Assess the morphology of the red blood cells.
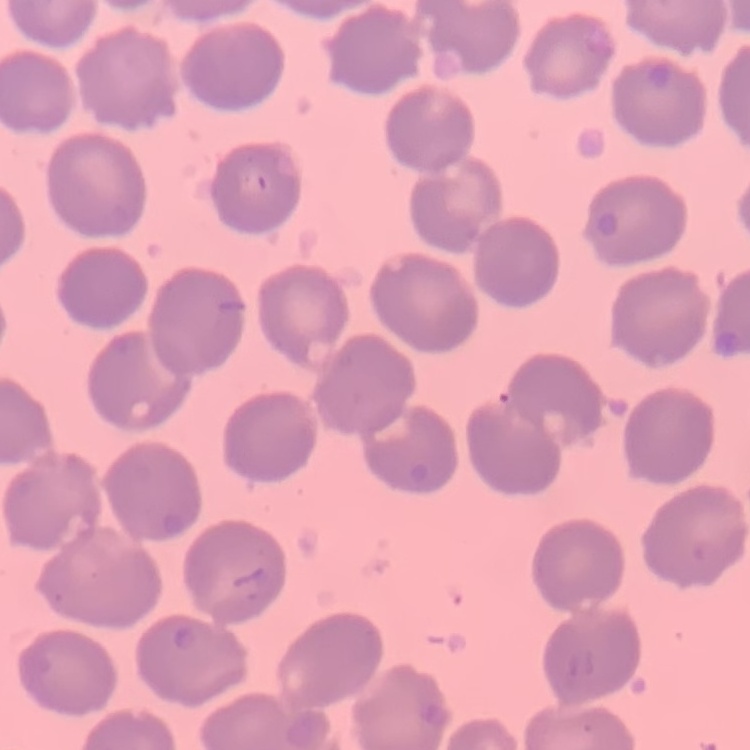
No rouleaux formation.

Summary:
  - Stain: Field's or Giemsa
  - Preparation: thin blood smear
  - Image type: one tile cut from a larger photomicrograph